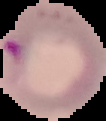
malaria_status: parasitized
preparation: thin blood film
image_size: 106×121 pixels
image_type: cell region segmented out of the field of view; surrounding area masked to black